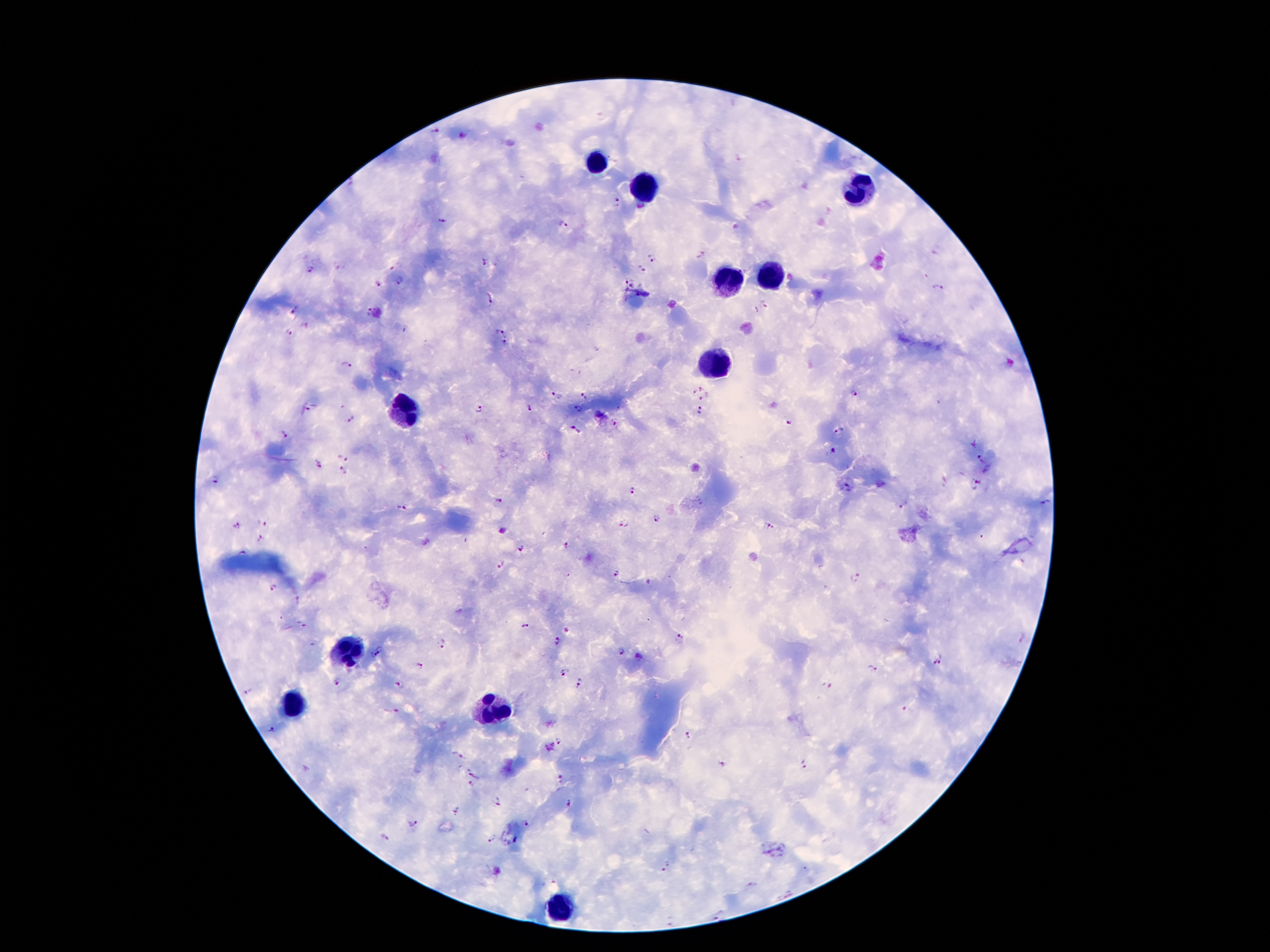

Approximate centers as [x, y] in pixels. Leukocyte locations: [596, 161], [643, 189], [856, 192], [727, 276], [769, 276], [716, 365], [401, 413], [349, 653], [291, 704], [492, 709], [564, 905]. Plasmodium parasite locations: [434, 133], [617, 203], [441, 220], [563, 224], [701, 255], [652, 256], [484, 264], [396, 266], [642, 269], [312, 270], [399, 282], [625, 282], [378, 283], [633, 283], [938, 288], [488, 297], [766, 305], [292, 308], [367, 312], [500, 329], [290, 333], [505, 343], [343, 364], [696, 389], [584, 393], [556, 396], [852, 396], [312, 405], [530, 408], [478, 409], [577, 409], [698, 410], [351, 421], [615, 422], [789, 422], [575, 429], [839, 432], [284, 435], [973, 445], [835, 451], [344, 454], [982, 460], [316, 463], [344, 473], [215, 481], [846, 486], [977, 486], [633, 489], [498, 502], [905, 507], [399, 508], [656, 518], [264, 522], [624, 523], [769, 525], [237, 526], [260, 539], [565, 546], [520, 549], [239, 553], [501, 568], [618, 574], [855, 575], [274, 589], [299, 601], [300, 627], [524, 627], [681, 639], [556, 642], [443, 643], [312, 644], [384, 647], [621, 652], [372, 657], [941, 659], [932, 663], [419, 668], [871, 670], [564, 673], [338, 682], [400, 683], [581, 685], [829, 685], [249, 691], [393, 712], [908, 712], [271, 731], [687, 737], [561, 741], [457, 755], [726, 766], [802, 766], [476, 773], [561, 777], [470, 786], [499, 802], [569, 802], [456, 811], [411, 824], [529, 824], [383, 836], [492, 838], [517, 842], [666, 866], [752, 886], [787, 895], [718, 916], [670, 920]. Image is 1270×952 pixels. Smartphone photograph taken through the microscope eyepiece. Thick blood film. One field from this slide. Patient malaria status: positive for Plasmodium falciparum. Giemsa-stained preparation. 100x magnification.